Evaluate for Plasmodium parasites.
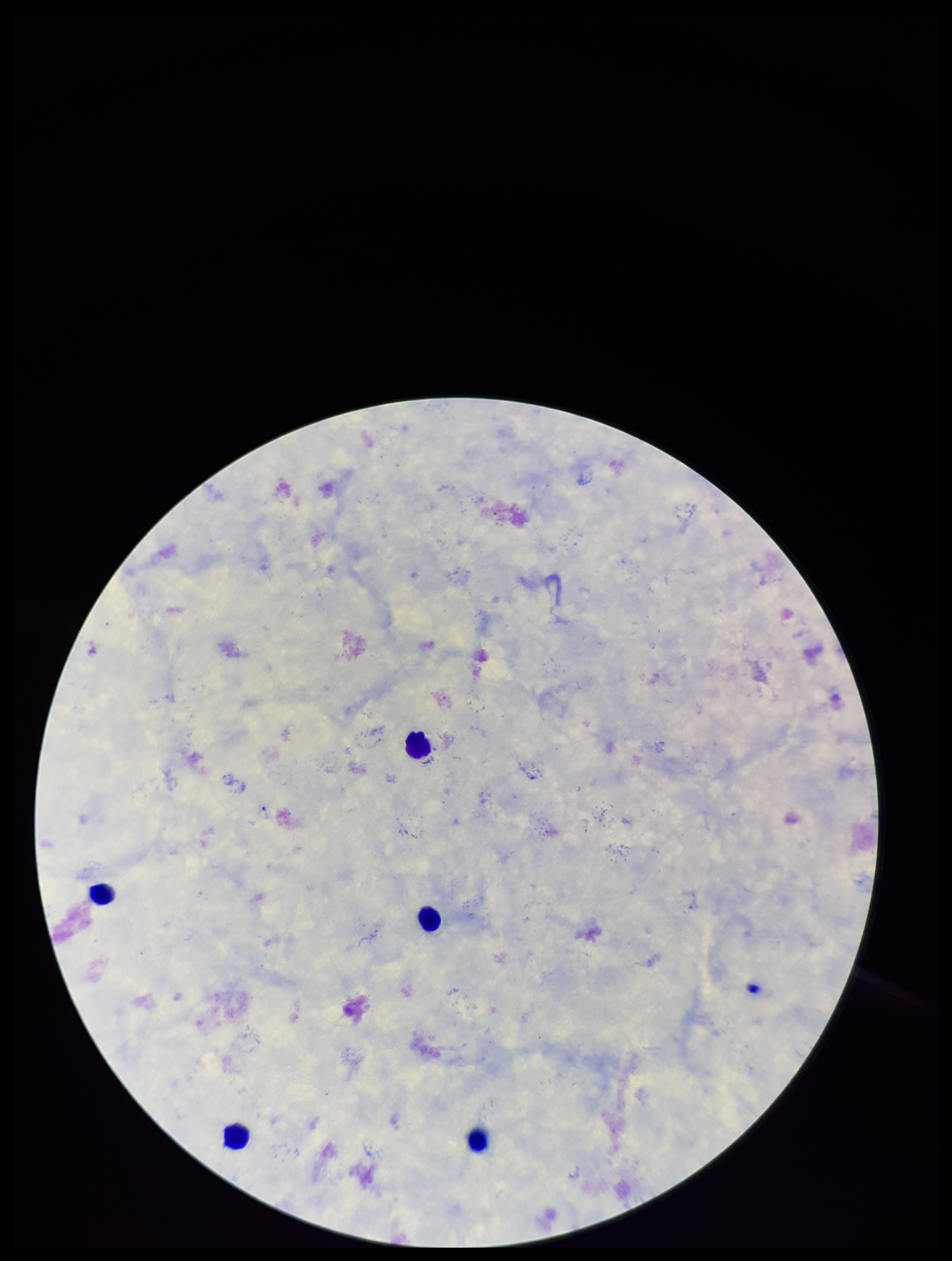

None identified.

stain = Giemsa
image size = 952×1261 pixels
field of view = one from this slide
leukocyte count = 4
capture = smartphone photograph through the microscope eyepiece
preparation = thick smear
patient malaria status = negative
parasite count = 0